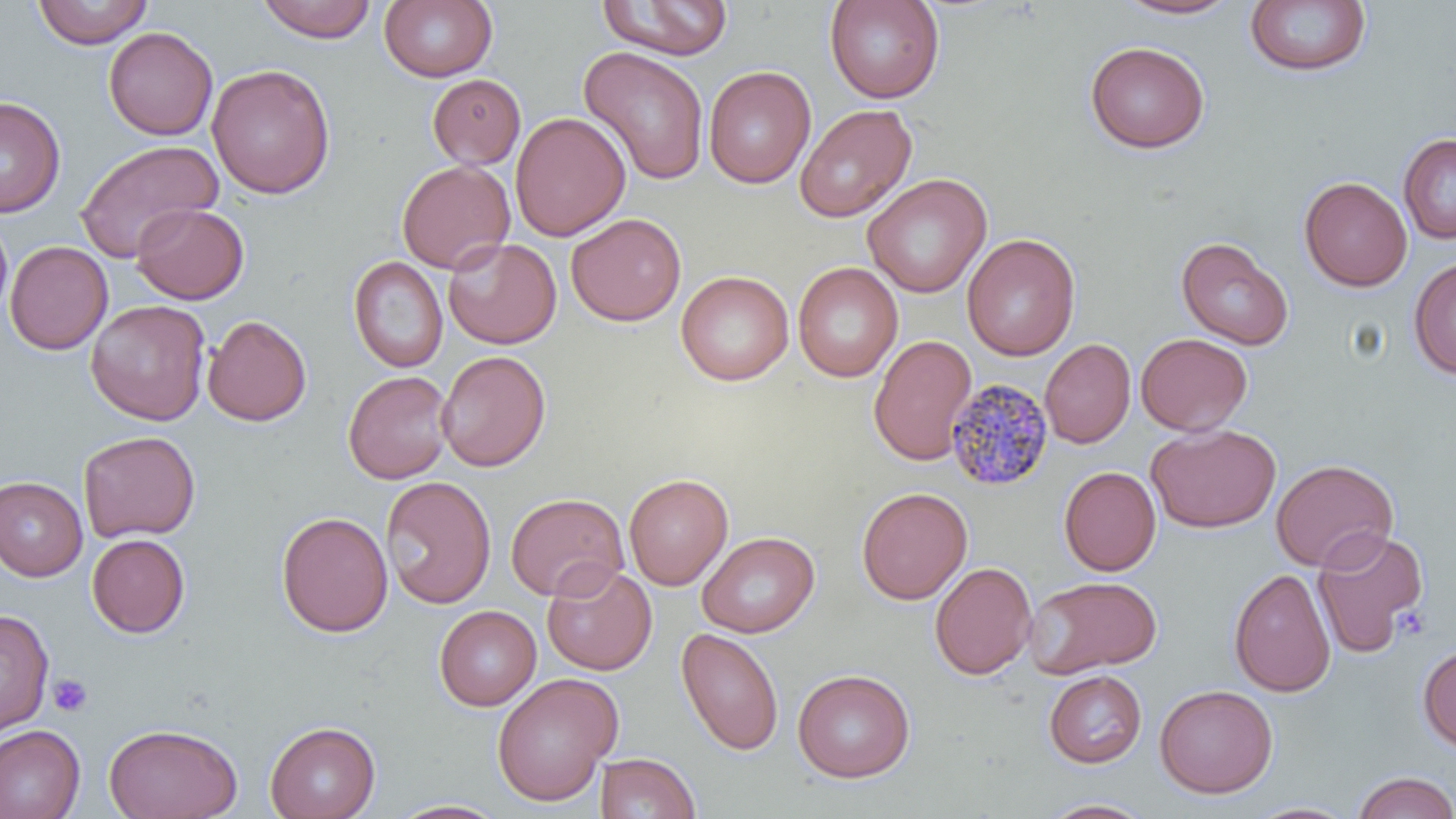
Summary:
  - Coordinate format: approximate bounding boxes as (x1,y1)-(x2,y2) corner pairs in pixels
  - Uninfected red blood cell locations: (32,0)-(153,48), (256,0)-(378,43), (379,0)-(497,82), (597,0)-(734,61), (825,0)-(945,103), (1113,1)-(1243,20), (1244,1)-(1371,78), (104,26)-(218,140), (1085,40)-(1210,154), (577,46)-(710,185), (207,64)-(336,200), (703,65)-(816,189), (427,74)-(526,169), (0,97)-(65,217), (795,103)-(917,223), (510,111)-(631,241), (1398,134)-(1456,244), (74,139)-(224,263), (396,159)-(515,274), (863,173)-(991,298), (1299,176)-(1412,291), (131,203)-(249,304), (566,213)-(686,326), (0,215)-(13,322), (962,233)-(1081,361), (443,237)-(562,349), (1176,237)-(1294,350), (5,241)-(113,355), (348,256)-(448,373), (1408,258)-(1456,380), (792,261)-(903,382), (676,270)-(794,386), (86,300)-(211,425), (202,314)-(312,426), (1136,333)-(1253,436), (868,335)-(977,466), (1040,339)-(1136,448), (435,350)-(551,472), (343,371)-(453,484), (1146,423)-(1281,533), (77,431)-(200,542), (1271,458)-(1399,572), (1059,467)-(1161,575), (623,473)-(733,590), (0,476)-(87,581), (380,476)-(496,609), (856,487)-(973,604), (505,493)-(628,601), (276,511)-(393,637), (1312,527)-(1429,657), (696,531)-(819,638), (87,534)-(190,638), (929,561)-(1037,680), (541,562)-(657,676), (1228,567)-(1336,697), (1024,575)-(1163,677), (434,605)-(541,711), (0,608)-(54,734), (676,627)-(784,756), (1417,643)-(1456,753), (792,668)-(915,782), (1043,669)-(1147,768), (491,672)-(622,806), (1154,684)-(1278,798), (264,721)-(380,819), (104,723)-(243,819), (0,725)-(84,819), (595,752)-(701,819), (1351,771)-(1456,819), (1037,797)-(1157,817), (386,798)-(510,818), (1244,801)-(1360,819)
  - Plasmodium malariae-infected red blood cell locations: (945,376)-(1055,492)
  - Platelet locations: (48,674)-(93,717)
  - Slide-level diagnosis: Plasmodium malariae
  - Modality: light microscopy
  - Preparation: thin blood smear
  - Magnification: 1000x
  - Stain: May-Grünwald-Giemsa
  - Image size: 1456×819 pixels
  - Field of view: single